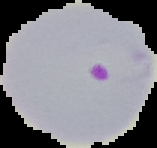
Summary:
  - Preparation: thin blood film
  - Malaria status: parasitized
  - Image size: 157×148 pixels
  - Image type: cell region segmented out of the field of view; surrounding area masked to black